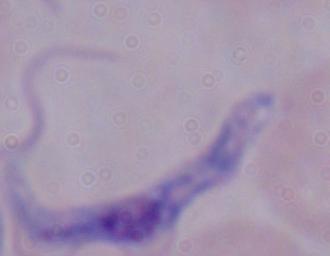

Summary:
  - Magnification: 1000x
  - Identification: trypanosome
  - Modality: photomicrograph